Give the extent of all uninfected red blood cells.
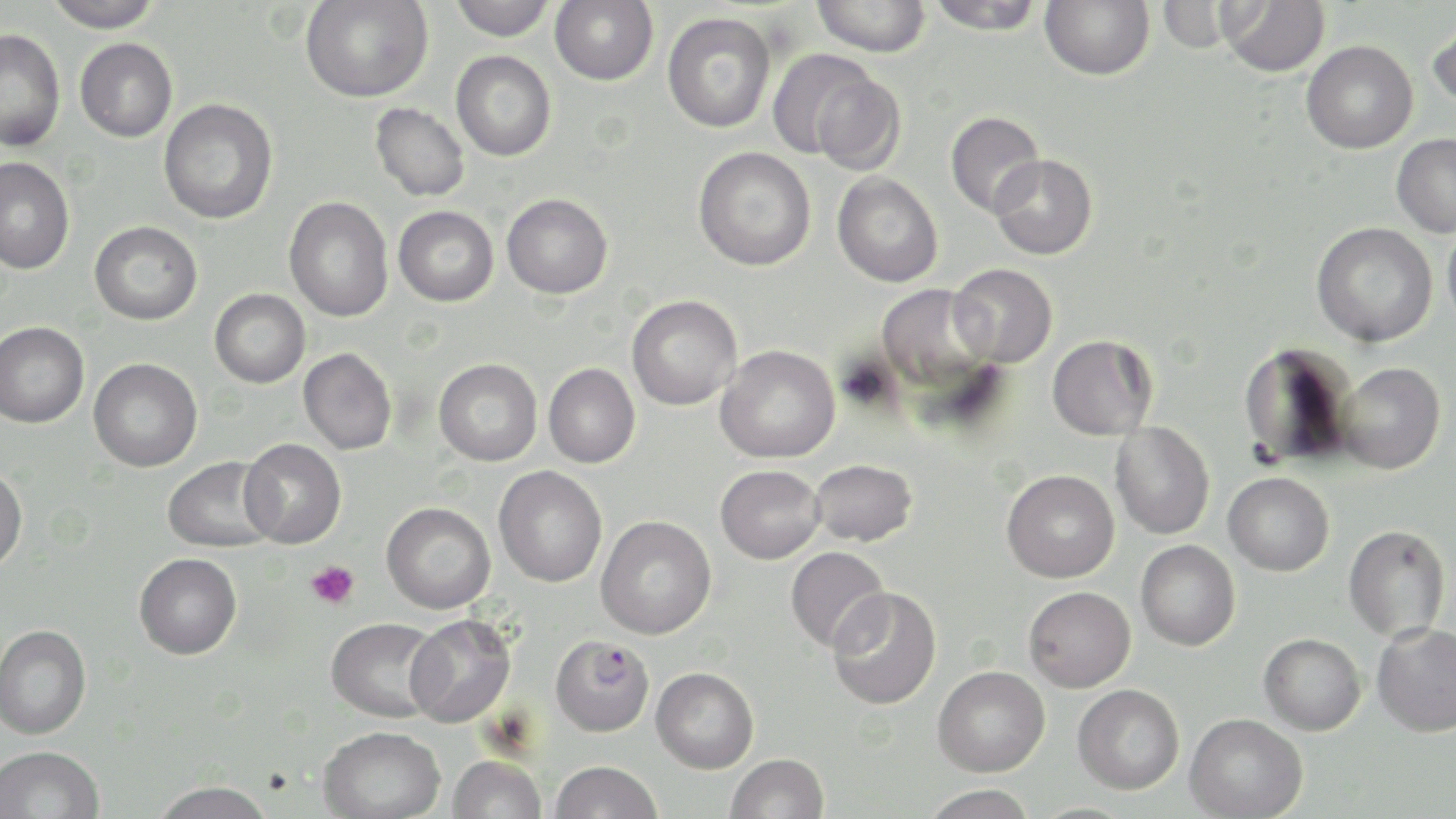
Approximate bounding boxes as [x1, y1, x2, y2] in pixels.
Uninfected red blood cells: [45, 0, 162, 32], [300, 0, 433, 103], [448, 0, 556, 41], [812, 0, 931, 56], [924, 0, 1046, 35], [1040, 0, 1154, 80], [550, 1, 659, 85], [1218, 1, 1330, 77], [662, 12, 776, 133], [1427, 17, 1456, 112], [0, 28, 66, 152], [75, 38, 178, 142], [1301, 40, 1418, 154], [766, 50, 889, 163], [451, 51, 556, 161], [809, 73, 908, 174], [158, 98, 278, 224], [370, 103, 470, 202], [945, 111, 1045, 218], [1392, 133, 1456, 237], [693, 147, 816, 271], [988, 154, 1097, 260], [0, 157, 74, 275], [832, 172, 943, 287], [501, 193, 613, 298], [283, 197, 394, 322], [393, 206, 498, 307], [1442, 218, 1456, 335], [89, 221, 203, 325], [1311, 222, 1438, 347], [948, 263, 1058, 367], [875, 284, 996, 399], [210, 288, 311, 388], [627, 295, 742, 410], [0, 321, 89, 427], [1047, 334, 1158, 440], [1237, 341, 1358, 468], [715, 345, 840, 463], [298, 347, 397, 454], [89, 358, 202, 472], [433, 358, 542, 466], [1336, 362, 1446, 474], [543, 363, 640, 467], [1109, 423, 1215, 539], [239, 438, 347, 549], [162, 457, 279, 553], [809, 459, 917, 547], [715, 464, 825, 564], [0, 465, 27, 573], [494, 465, 607, 587], [1002, 469, 1119, 583], [1223, 472, 1334, 576], [381, 502, 496, 614], [595, 515, 717, 639], [1343, 524, 1451, 642], [1136, 540, 1240, 651], [785, 546, 891, 653], [134, 552, 242, 659], [1023, 586, 1136, 692], [827, 587, 942, 710], [405, 615, 516, 727], [326, 617, 443, 722], [1372, 622, 1456, 736], [0, 624, 91, 739], [1258, 633, 1366, 735], [932, 665, 1050, 776], [651, 667, 759, 773], [1072, 684, 1184, 794], [1185, 713, 1308, 818], [317, 725, 445, 819], [0, 744, 105, 819], [726, 753, 829, 818], [447, 755, 547, 819], [549, 760, 663, 819], [150, 780, 277, 819], [920, 784, 1037, 819].

Summary:
  - Plasmodium falciparum-infected red blood cell locations: [550, 634, 655, 737]
  - Platelet locations: [305, 561, 359, 609]
  - Slide-level diagnosis: Plasmodium falciparum
  - Field of view: one of a larger specimen
  - Image size: 1456×819 pixels
  - Modality: light microscopy
  - Magnification: 1000x
  - Preparation: thin blood smear
  - Stain: May-Grünwald-Giemsa